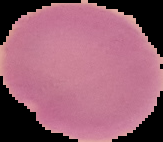

{
  "preparation": "thin blood film",
  "malaria_status": "uninfected",
  "image_type": "segmented cell region on a black background",
  "image_size": "163×142 pixels"
}